Name the parasite shown.
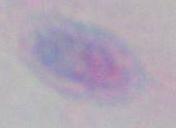
Toxoplasma gondii.

Captured at 1000x magnification. Photomicrograph.